Outline each Plasmodium vivax-infected red blood cell.
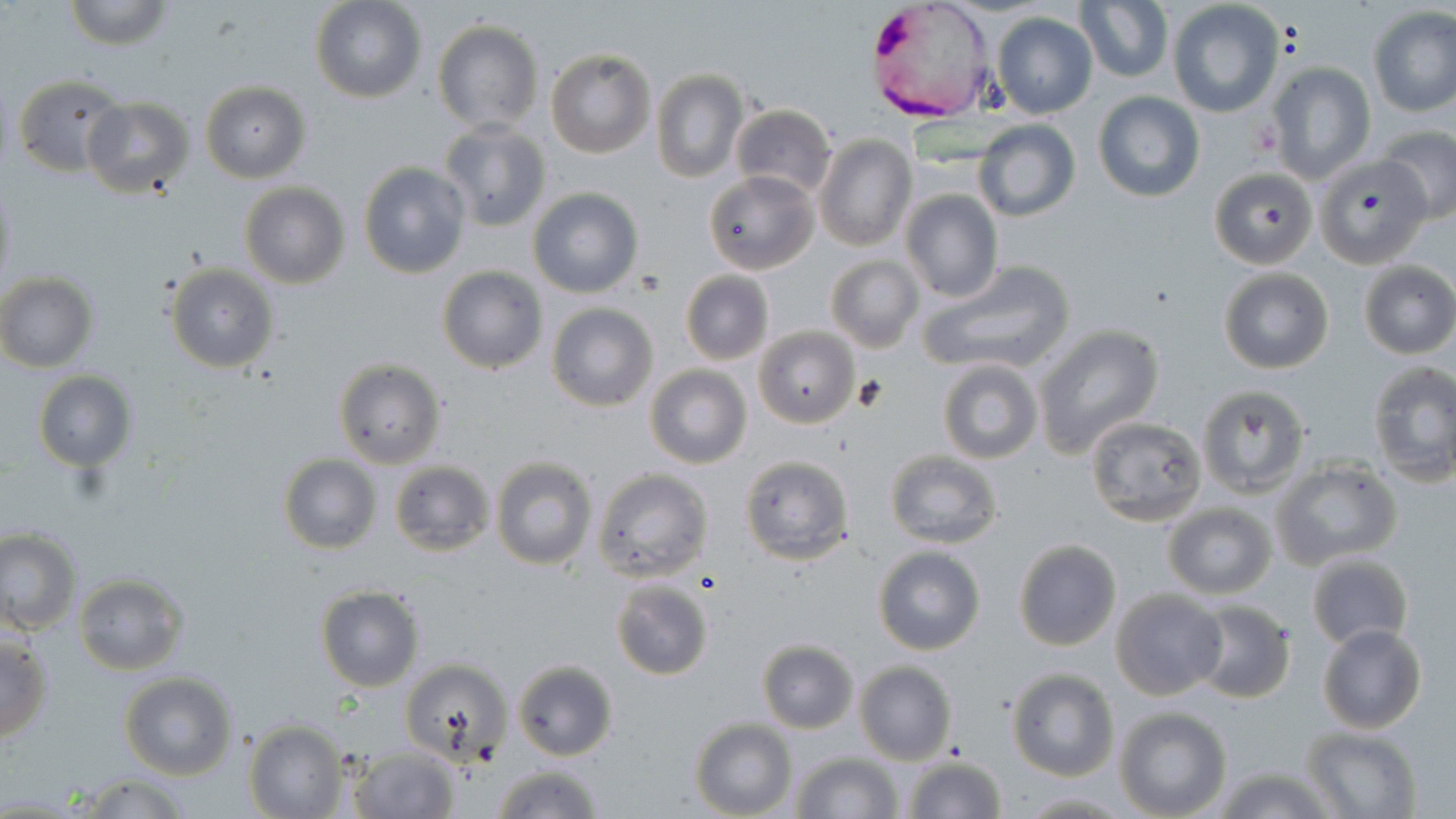

Approximate bounding boxes as named x1/y1/x2/y2 corners in pixels.
Plasmodium vivax-infected red blood cells: (x1=865, y1=1, x2=990, y2=128).

Platelet locations: (x1=1248, y1=122, x2=1281, y2=158), (x1=850, y1=376, x2=889, y2=412). Uninfected red blood cell locations: (x1=60, y1=0, x2=177, y2=50), (x1=310, y1=0, x2=427, y2=104), (x1=1076, y1=1, x2=1172, y2=84), (x1=1167, y1=2, x2=1286, y2=117), (x1=1367, y1=7, x2=1456, y2=117), (x1=991, y1=12, x2=1098, y2=119), (x1=432, y1=20, x2=543, y2=133), (x1=545, y1=48, x2=655, y2=159), (x1=1265, y1=61, x2=1375, y2=185), (x1=651, y1=69, x2=749, y2=184), (x1=12, y1=72, x2=127, y2=178), (x1=200, y1=80, x2=312, y2=183), (x1=1093, y1=92, x2=1205, y2=204), (x1=81, y1=97, x2=194, y2=197), (x1=730, y1=105, x2=836, y2=200), (x1=973, y1=120, x2=1081, y2=221), (x1=438, y1=121, x2=551, y2=232), (x1=1376, y1=126, x2=1456, y2=225), (x1=376, y1=133, x2=506, y2=255), (x1=812, y1=133, x2=917, y2=254), (x1=1314, y1=155, x2=1430, y2=267), (x1=358, y1=162, x2=470, y2=278), (x1=1208, y1=167, x2=1319, y2=269), (x1=703, y1=169, x2=819, y2=276), (x1=0, y1=179, x2=17, y2=298), (x1=239, y1=182, x2=349, y2=289), (x1=527, y1=187, x2=644, y2=298), (x1=900, y1=190, x2=1003, y2=303), (x1=825, y1=254, x2=922, y2=353), (x1=919, y1=259, x2=1075, y2=376), (x1=1357, y1=261, x2=1456, y2=359), (x1=164, y1=263, x2=280, y2=373), (x1=437, y1=265, x2=548, y2=375), (x1=1218, y1=267, x2=1334, y2=374), (x1=680, y1=270, x2=774, y2=365), (x1=0, y1=272, x2=99, y2=372), (x1=546, y1=302, x2=658, y2=411), (x1=1033, y1=324, x2=1165, y2=459), (x1=755, y1=325, x2=859, y2=428), (x1=334, y1=358, x2=447, y2=470), (x1=936, y1=359, x2=1045, y2=465), (x1=1367, y1=360, x2=1456, y2=486), (x1=644, y1=364, x2=752, y2=470), (x1=33, y1=370, x2=137, y2=471), (x1=1195, y1=385, x2=1310, y2=496), (x1=1084, y1=416, x2=1208, y2=529), (x1=883, y1=449, x2=1004, y2=549), (x1=738, y1=453, x2=855, y2=567), (x1=279, y1=455, x2=381, y2=554), (x1=489, y1=456, x2=599, y2=571), (x1=1270, y1=457, x2=1403, y2=571), (x1=389, y1=460, x2=495, y2=556), (x1=590, y1=467, x2=714, y2=584), (x1=1162, y1=501, x2=1279, y2=599), (x1=0, y1=527, x2=81, y2=635), (x1=1012, y1=539, x2=1123, y2=652), (x1=872, y1=546, x2=987, y2=656), (x1=1305, y1=550, x2=1414, y2=654), (x1=74, y1=573, x2=189, y2=675), (x1=609, y1=578, x2=715, y2=681), (x1=315, y1=585, x2=425, y2=693), (x1=1109, y1=588, x2=1227, y2=701), (x1=1190, y1=599, x2=1296, y2=703), (x1=1316, y1=623, x2=1428, y2=733), (x1=0, y1=634, x2=53, y2=743), (x1=755, y1=638, x2=860, y2=733), (x1=399, y1=657, x2=512, y2=765), (x1=513, y1=660, x2=619, y2=761), (x1=854, y1=661, x2=958, y2=764), (x1=1006, y1=667, x2=1118, y2=781), (x1=119, y1=672, x2=237, y2=780), (x1=1114, y1=707, x2=1231, y2=819), (x1=243, y1=719, x2=350, y2=818), (x1=688, y1=719, x2=796, y2=818), (x1=1300, y1=726, x2=1423, y2=818), (x1=345, y1=744, x2=463, y2=818), (x1=791, y1=750, x2=902, y2=819), (x1=900, y1=754, x2=1009, y2=819), (x1=492, y1=762, x2=603, y2=819), (x1=1211, y1=764, x2=1335, y2=819), (x1=69, y1=773, x2=195, y2=818), (x1=1014, y1=791, x2=1131, y2=816). Slide-level diagnosis: Plasmodium vivax. May-Grünwald-Giemsa stain. Captured at 1000x magnification. Optical microscopy. Thin blood film. Single field of view. Image is 1456×819 pixels.